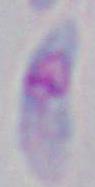
Summary:
  - Identification: Toxoplasma gondii
  - Modality: micrograph
  - Magnification: 1000x